Report the malaria status of this cell.
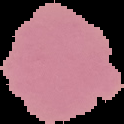
It is uninfected.

Image is 124×124 pixels. The area outside the segmented cell region is set to black. From a thin blood smear.